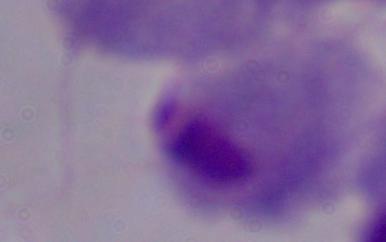
Summary:
  - Identification: trichomonad
  - Modality: micrograph
  - Magnification: 1000x